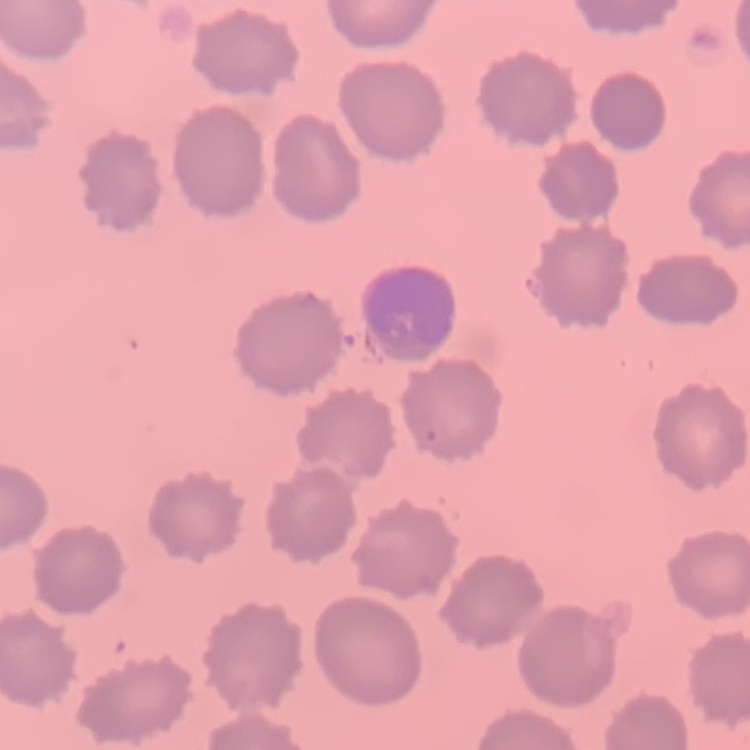

Summary:
  - Red blood cell morphology: no rouleaux formation
  - Preparation: thin blood smear
  - Image type: one tile cut from a larger photomicrograph
  - Stain: Field's or Giemsa